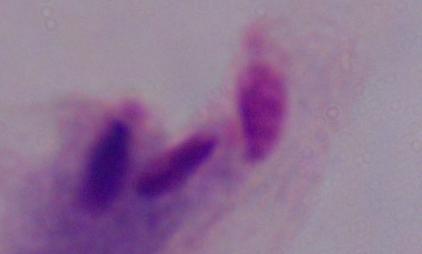

Summary:
  - Modality: micrograph
  - Magnification: 1000x
  - Identification: trichomonad